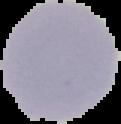

image type = cell region segmented out of the field of view; surrounding area masked to black
malaria status = uninfected
preparation = thin blood film
image size = 121×124 pixels